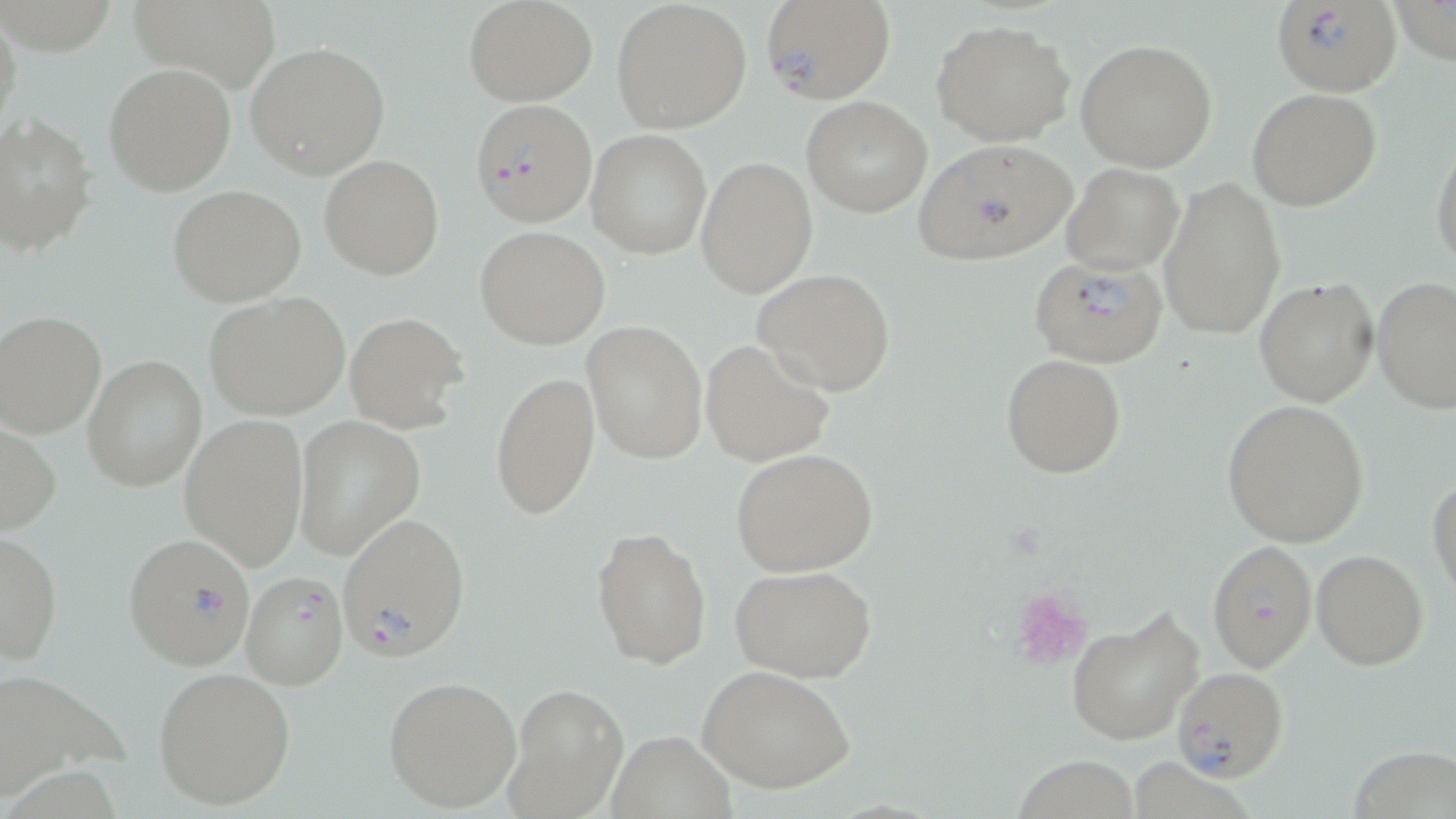

Approximate bounding boxes as [x1, y1, x2, y2] in pixels. Uninfected red blood cell locations: [125, 0, 284, 93], [464, 0, 599, 104], [1389, 0, 1456, 63], [609, 1, 752, 133], [0, 10, 22, 140], [930, 18, 1076, 147], [1076, 37, 1219, 173], [245, 40, 391, 179], [103, 62, 238, 197], [1247, 88, 1381, 212], [802, 96, 933, 218], [0, 114, 97, 257], [585, 129, 712, 258], [1430, 133, 1456, 270], [590, 142, 818, 278], [696, 154, 818, 298], [319, 155, 445, 280], [1062, 164, 1184, 275], [1158, 175, 1286, 342], [168, 184, 306, 306], [476, 226, 611, 350], [753, 268, 897, 396], [1371, 277, 1456, 413], [1254, 278, 1380, 407], [203, 292, 351, 420], [0, 311, 105, 437], [344, 311, 469, 432], [582, 321, 709, 464], [701, 338, 835, 467], [82, 354, 206, 492], [1001, 354, 1126, 477], [491, 371, 600, 522], [1223, 399, 1369, 546], [179, 414, 311, 571], [292, 415, 424, 560], [0, 419, 61, 536], [731, 448, 880, 577], [1427, 475, 1456, 599], [590, 526, 711, 672], [0, 529, 62, 666], [1310, 549, 1429, 670], [731, 565, 879, 683], [1065, 605, 1206, 747], [0, 664, 123, 798], [699, 665, 856, 794], [153, 666, 298, 811], [383, 675, 522, 813], [505, 684, 626, 817], [607, 732, 735, 817], [1347, 739, 1456, 819], [1016, 753, 1138, 819], [1127, 755, 1264, 819]. Platelet locations: [1011, 587, 1093, 672]. Plasmodium falciparum-infected red blood cell locations: [759, 0, 897, 107], [1271, 0, 1402, 96], [469, 97, 595, 226], [911, 140, 1079, 267], [1028, 254, 1170, 368], [338, 511, 471, 662], [124, 533, 252, 670], [1207, 541, 1316, 671], [240, 571, 349, 690], [1170, 666, 1287, 783]. Slide-level diagnosis: Plasmodium falciparum. May-Grünwald-Giemsa-stained preparation. Image is 1456×819 pixels. One field of a larger specimen. Thin blood smear. Optical microscopy. 1000x magnification.